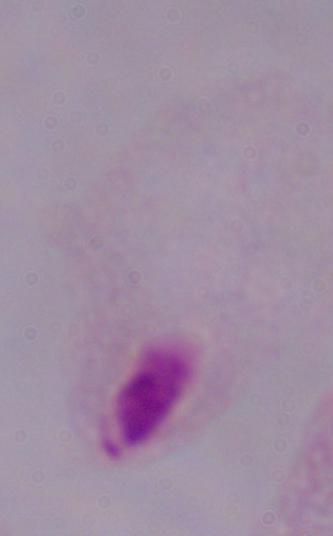

identification: trichomonad
modality: micrograph
magnification: 1000x